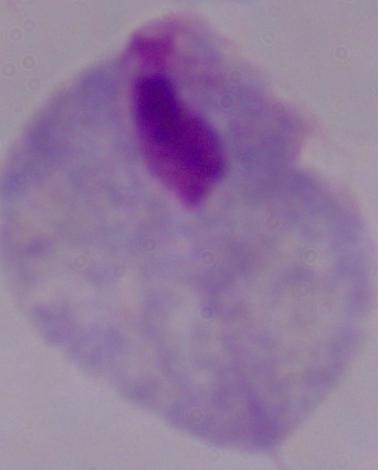
modality: micrograph
identification: trichomonad
magnification: 1000x